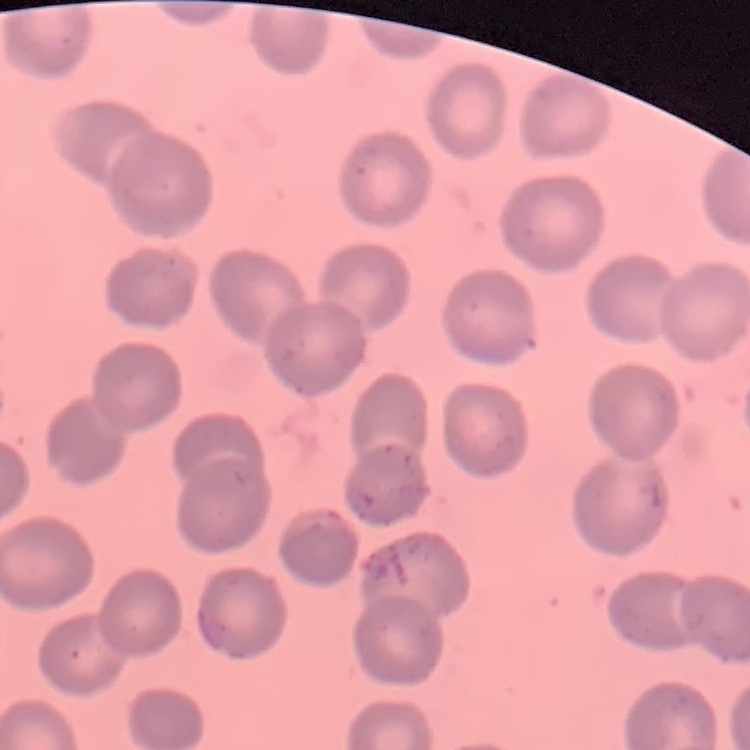
erythrocyte morphology = no rouleaux formation
preparation = thin blood smear
image type = square crop of a larger photomicrograph
stain = Field's or Giemsa